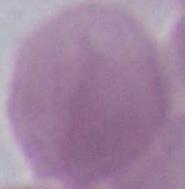
A red blood cell is seen. Micrograph. 1000x magnification.